Describe the morphology of the erythrocytes.
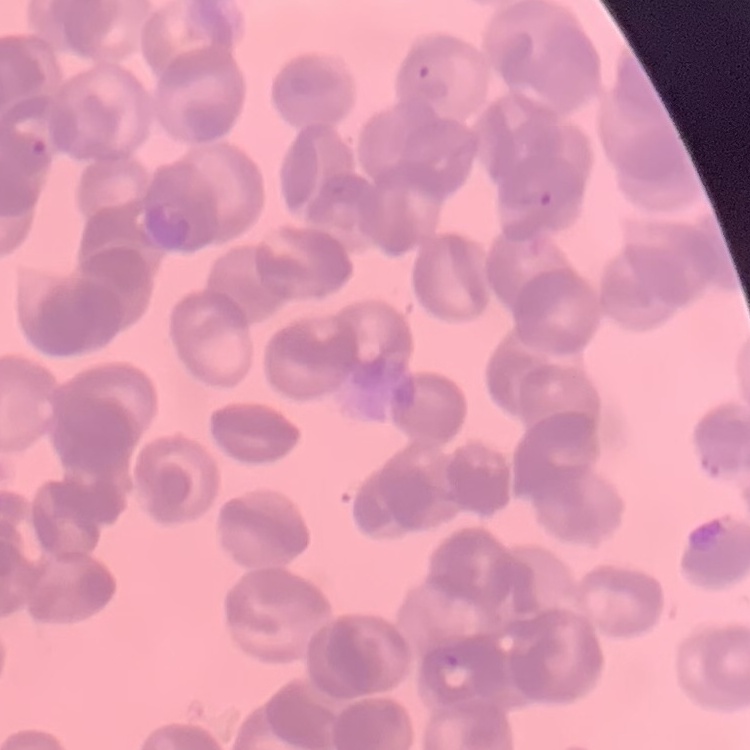

Rouleaux formation.

Summary:
  - Stain: Field's or Giemsa
  - Image type: square crop of a larger photomicrograph
  - Preparation: thin blood smear